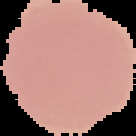 Image is 136×136 pixels. Result: no Plasmodium parasites detected. The area outside the segmented cell region is set to black. From a thin blood film.